Comment on the morphology of the erythrocytes.
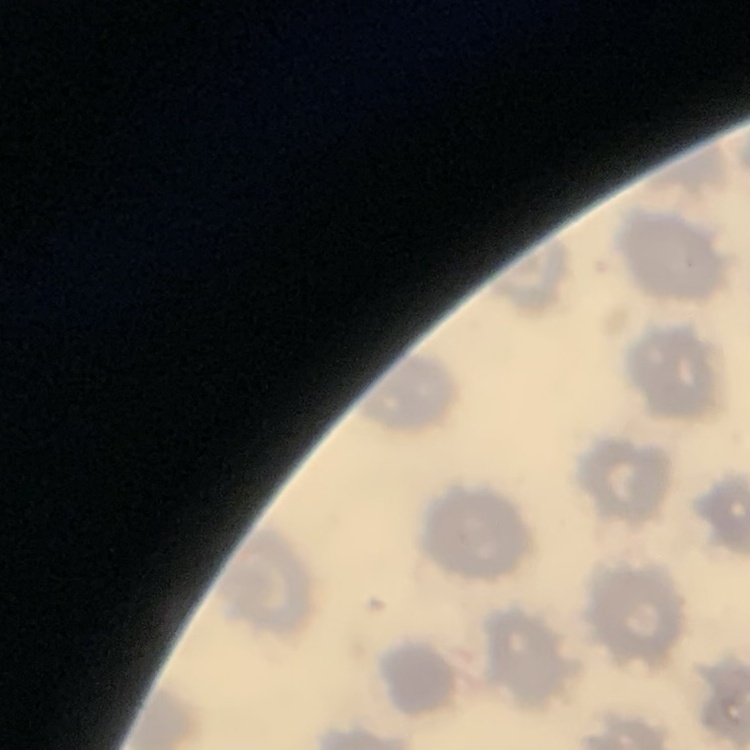
They show no rouleaux formation.

preparation = thin blood smear
stain = Field's or Giemsa
image type = square crop of a larger photomicrograph